Assess this cell for malaria.
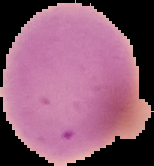
Uninfected.

The area outside the segmented cell region is set to black. Image is 154×166 pixels. From a thin blood film.